Evaluate for malaria.
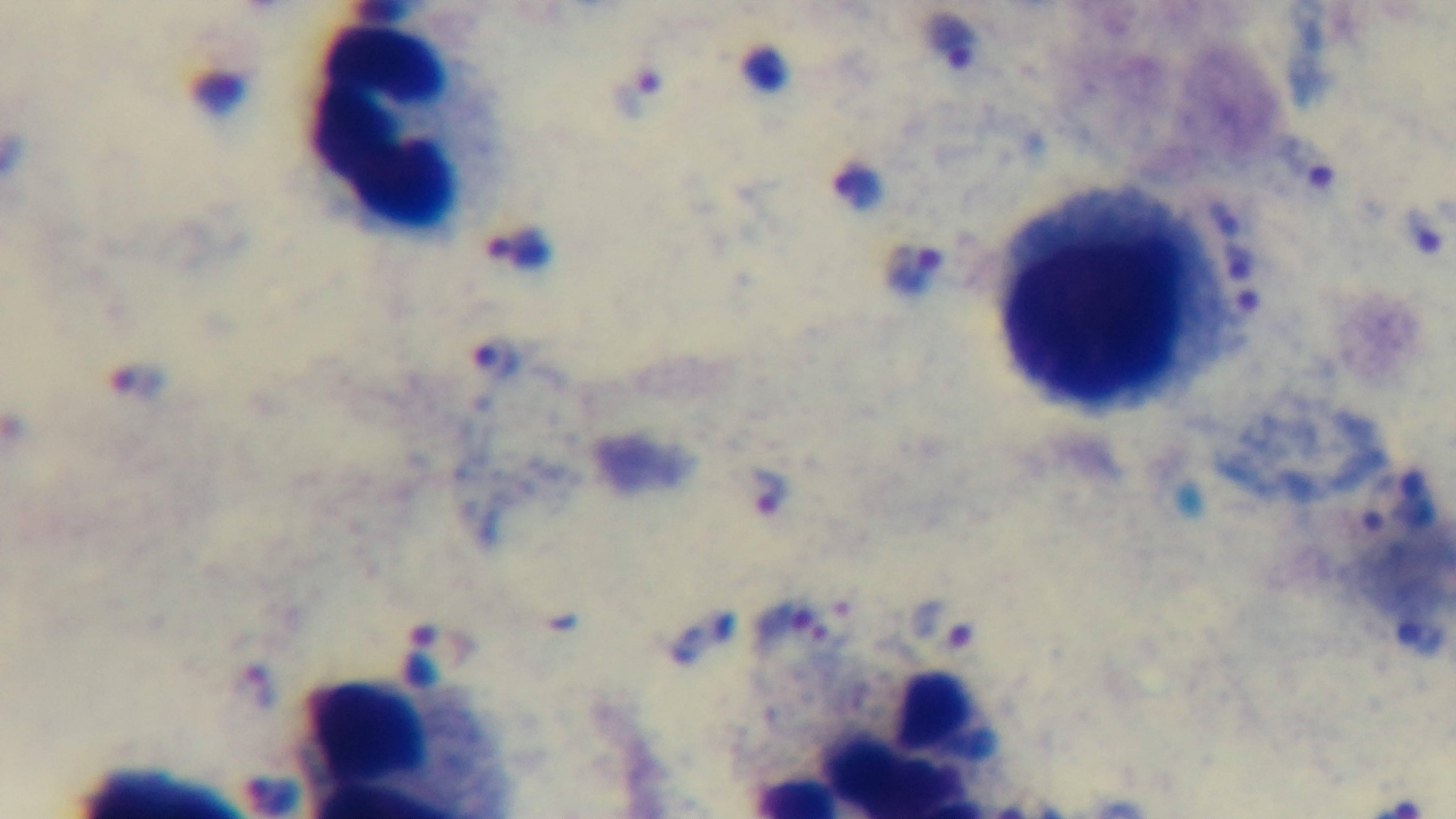

Positive.

Summary:
  - Stain: Giemsa
  - Objective: 100x oil immersion
  - Field of view: single
  - Capture: mounted 4K digital camera
  - Preparation: thick
  - Modality: light microscopy